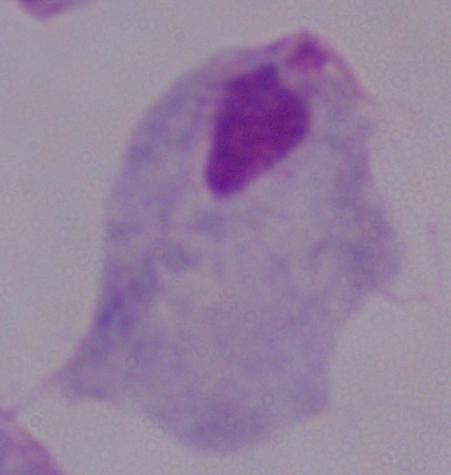

modality = photomicrograph
identification = trichomonad
magnification = 1000x